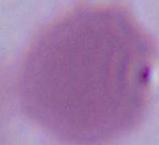

Summary:
  - Magnification: 1000x
  - Modality: micrograph
  - Identification: red blood cell